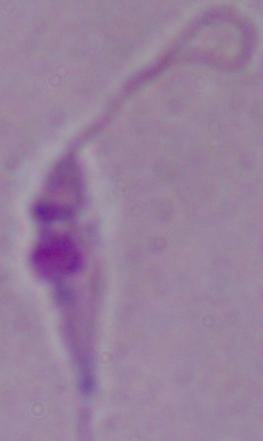

Summary:
  - Identification: Leishmania
  - Magnification: 1000x
  - Modality: photomicrograph